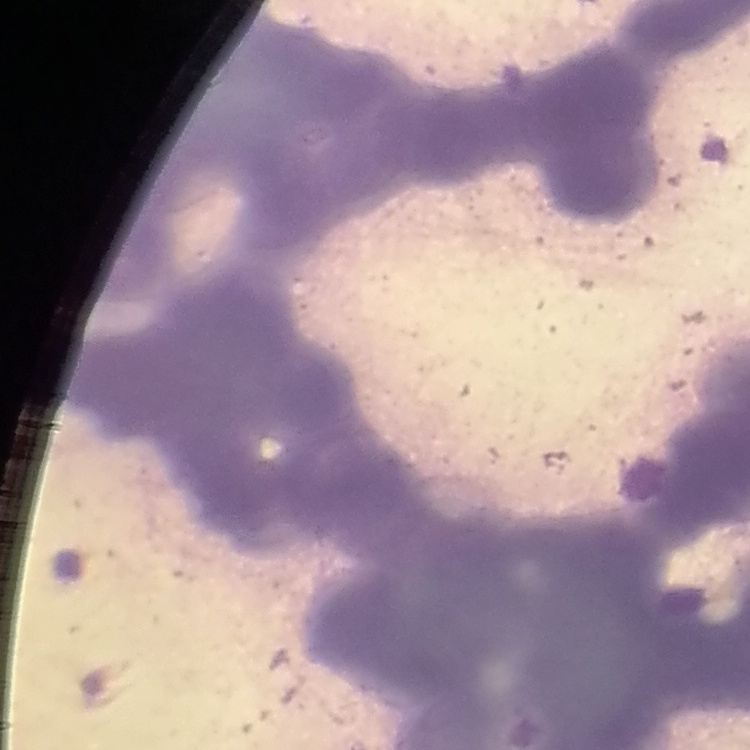

{
  "erythrocyte_morphology": "rouleaux formation",
  "stain": "Field's or Giemsa",
  "preparation": "thin blood smear",
  "image_type": "square crop of a larger photomicrograph"
}